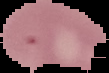

Summary:
  - Image size: 109×73 pixels
  - Image type: segmented cell region on a black background
  - Malaria status: parasitized
  - Preparation: thin blood smear